State which parasite is depicted.
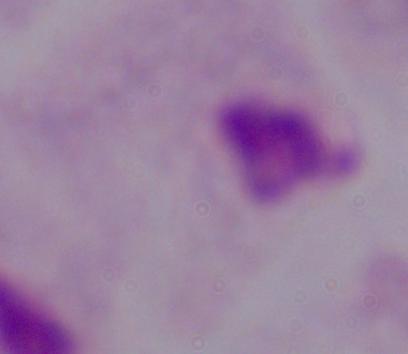
This is a trichomonad.

Captured at 1000x magnification. Photomicrograph.